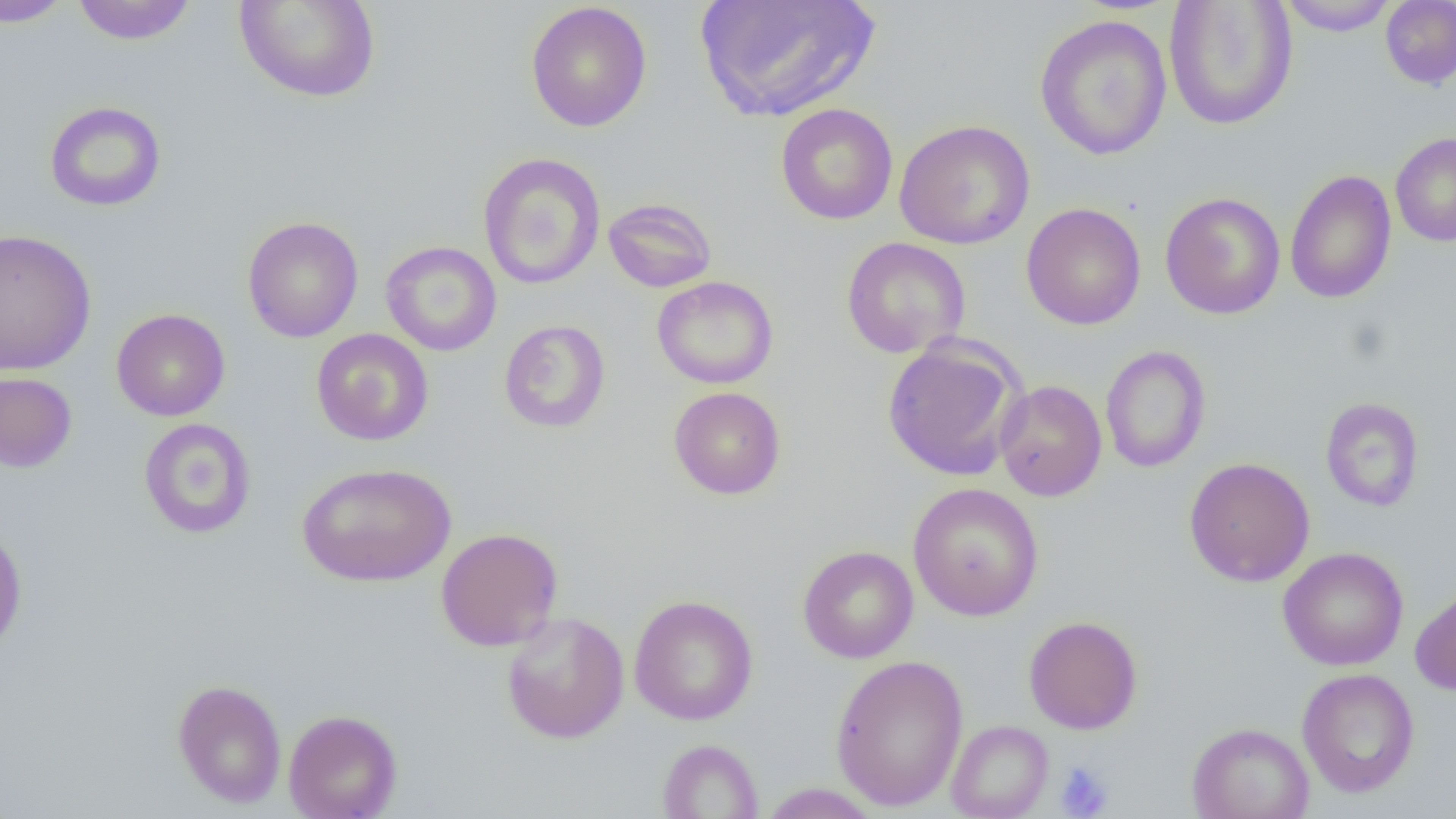
slide-level diagnosis = no evidence of blood parasites
field of view = one of a larger specimen
preparation = thin blood smear
image size = 1456×819 pixels
platelet locations = approximate bounding boxes as (x1,y1)-(x2,y2) corner pairs in pixels: (1054,760)-(1115,818)
uninfected red blood cell locations = approximate bounding boxes as (x1,y1)-(x2,y2) corner pairs in pixels: (1,0)-(74,28), (71,0)-(198,45), (234,0)-(381,103), (1278,0)-(1398,36), (1380,0)-(1456,89), (693,1)-(881,122), (1163,1)-(1298,130), (525,2)-(653,133), (1034,14)-(1173,161), (44,101)-(166,211), (775,103)-(899,225), (894,119)-(1035,250), (1390,132)-(1456,247), (478,152)-(606,290), (1284,169)-(1396,304), (1160,192)-(1285,320), (602,197)-(717,293), (1021,202)-(1146,330), (242,216)-(364,342), (0,228)-(97,376), (841,237)-(971,358), (380,241)-(501,357), (651,276)-(779,389), (112,308)-(230,421), (498,319)-(611,433), (311,328)-(434,446), (881,335)-(1026,481), (1099,345)-(1211,473), (0,371)-(77,473), (995,379)-(1107,501), (668,386)-(786,500), (1320,397)-(1425,512), (138,418)-(256,539), (1184,457)-(1315,587), (297,461)-(456,588), (907,482)-(1045,622), (0,522)-(28,657), (435,527)-(564,652), (797,545)-(918,663), (1277,546)-(1409,671), (1410,580)-(1456,697), (629,594)-(759,725), (501,611)-(630,744), (1023,615)-(1143,734), (829,654)-(969,811), (1297,668)-(1420,798), (172,679)-(287,808), (284,709)-(402,819), (946,720)-(1053,819), (1187,722)-(1314,819), (656,739)-(763,818), (757,783)-(882,818)
modality = light microscopy
magnification = 1000x